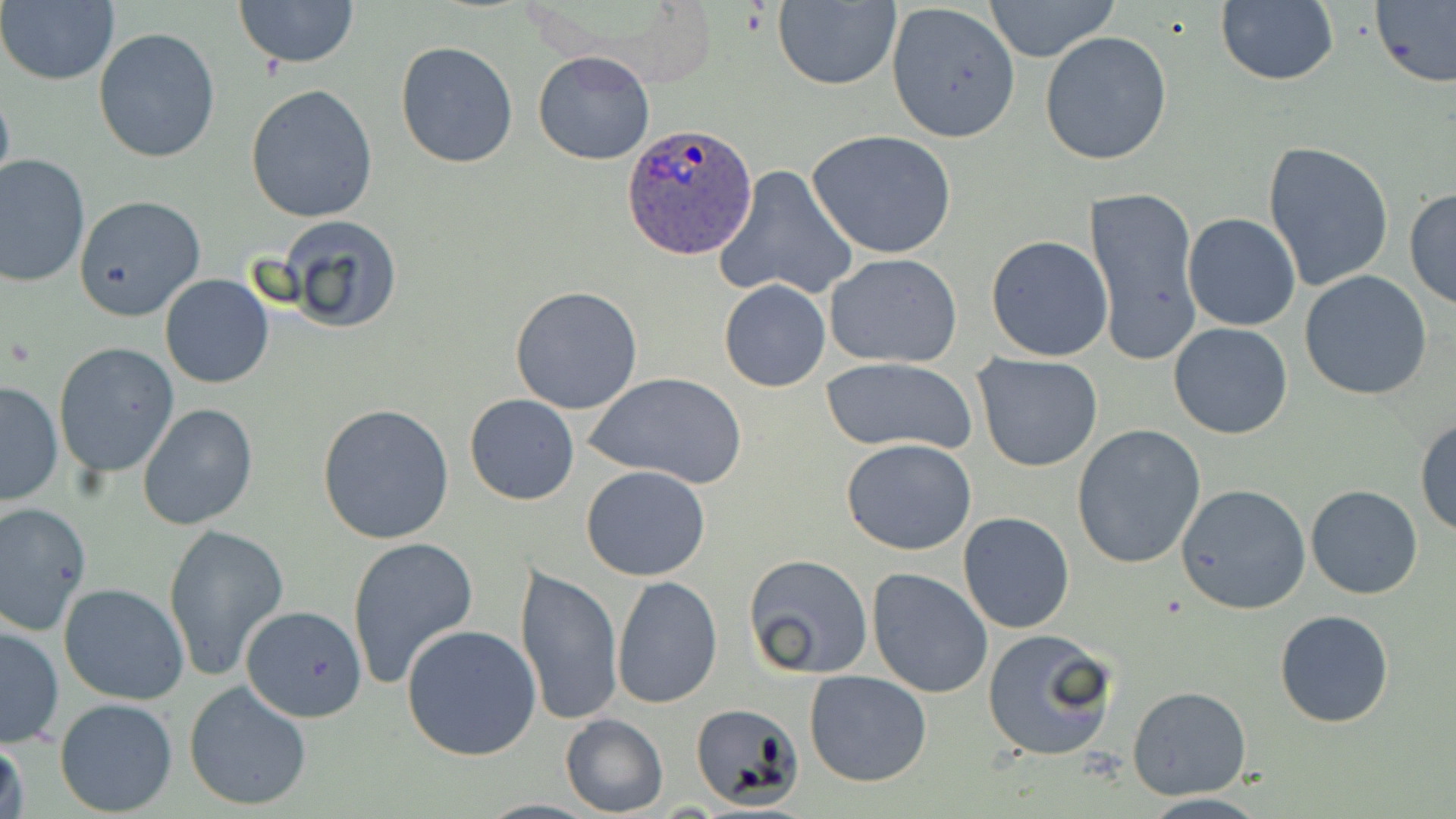
Summary:
  - Coordinate format: approximate bounding boxes as (x1,y1)-(x2,y2) corner pairs in pixels
  - Uninfected red blood cell locations: (234,0)-(358,70), (982,0)-(1121,62), (1,1)-(119,86), (772,1)-(900,90), (1214,1)-(1340,89), (1371,1)-(1456,89), (885,2)-(1021,142), (93,28)-(221,163), (1040,32)-(1172,165), (395,41)-(520,169), (533,50)-(655,166), (0,79)-(15,203), (245,83)-(378,223), (808,129)-(958,261), (1263,141)-(1395,294), (0,154)-(90,288), (714,165)-(859,303), (1083,184)-(1201,368), (1404,189)-(1456,310), (73,194)-(207,322), (1183,213)-(1300,331), (278,214)-(406,335), (984,235)-(1113,360), (824,253)-(964,368), (1298,270)-(1433,401), (159,273)-(274,389), (718,278)-(833,392), (509,285)-(643,415), (1168,322)-(1294,440), (53,342)-(181,479), (973,353)-(1104,471), (823,358)-(978,455), (589,372)-(744,491), (1,379)-(64,505), (464,393)-(579,505), (138,403)-(259,531), (317,403)-(457,545), (1414,416)-(1456,535), (1071,423)-(1207,569), (841,438)-(979,557), (581,465)-(711,581), (1175,483)-(1311,615), (1305,485)-(1424,599), (1,501)-(92,634), (958,511)-(1075,634), (164,522)-(289,681), (347,535)-(478,691), (743,553)-(874,679), (516,562)-(623,727), (867,567)-(993,697), (610,576)-(723,706), (57,582)-(188,705), (239,607)-(366,727), (1274,610)-(1394,729), (1,623)-(65,749), (402,625)-(542,761), (982,628)-(1120,762), (803,670)-(932,788), (183,681)-(312,812), (1127,686)-(1252,800), (53,698)-(179,816), (692,700)-(807,808), (559,713)-(668,817), (1,725)-(30,819), (1134,793)-(1273,819)
  - Plasmodium ovale-infected red blood cell locations: (621,123)-(760,261)
  - Slide-level diagnosis: Plasmodium ovale
  - Field of view: single
  - Modality: light microscopy
  - Preparation: thin blood smear
  - Stain: May-Grünwald-Giemsa
  - Magnification: 1000x
  - Image size: 1456×819 pixels